Comment on the morphology of the erythrocytes.
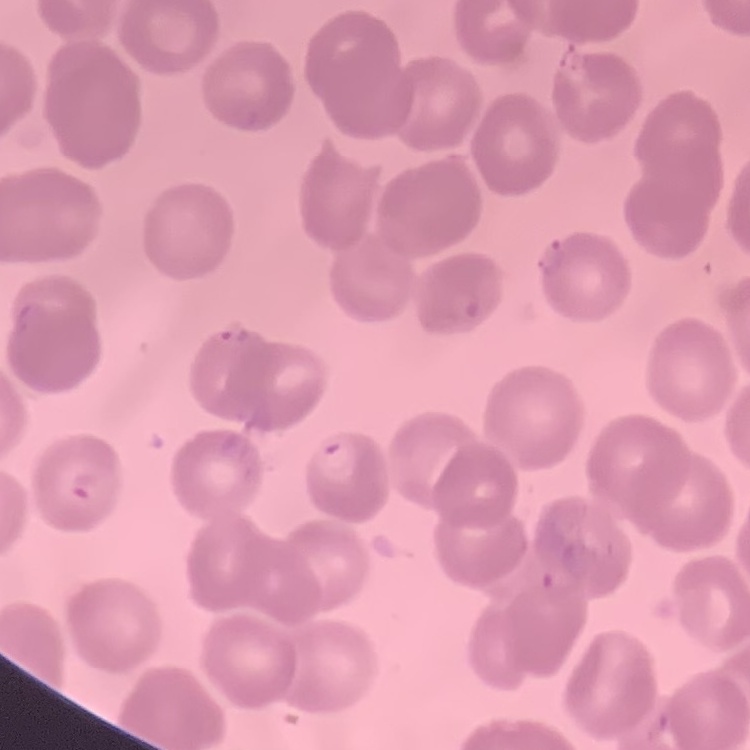
No rouleaux formation.

Summary:
  - Preparation: thin blood smear
  - Image type: square crop of a larger photomicrograph
  - Stain: Field's or Giemsa